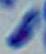

identification = Toxoplasma gondii
modality = micrograph
magnification = 1000x